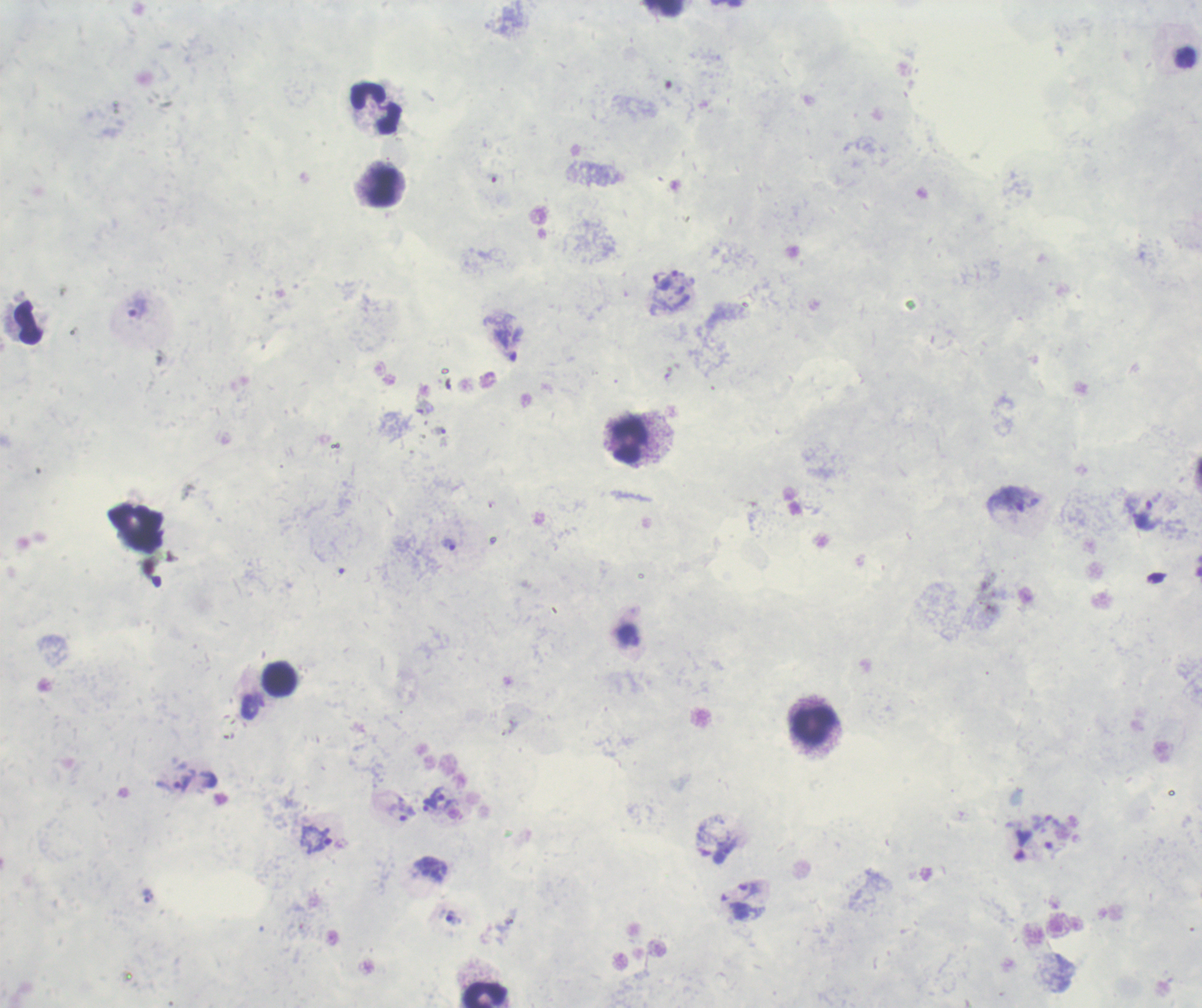
Approximate centers as [x, y] in pixels. Trophozoite locations: [138, 309], [1007, 500], [1144, 513], [448, 545], [174, 781], [446, 800], [429, 803], [402, 809], [315, 839], [726, 851], [747, 890], [452, 916]. Leukocyte locations: [663, 8], [376, 108], [383, 185], [29, 322], [627, 440], [136, 527], [279, 678], [813, 725], [485, 996]. Background quality: poor. Coloration quality: bad. Romanowsky stain. Previously used in an actual diagnosis. Thick blood film. One field from this slide. Image is 1202×1008 pixels. 100x magnification. Result: malaria parasites detected.